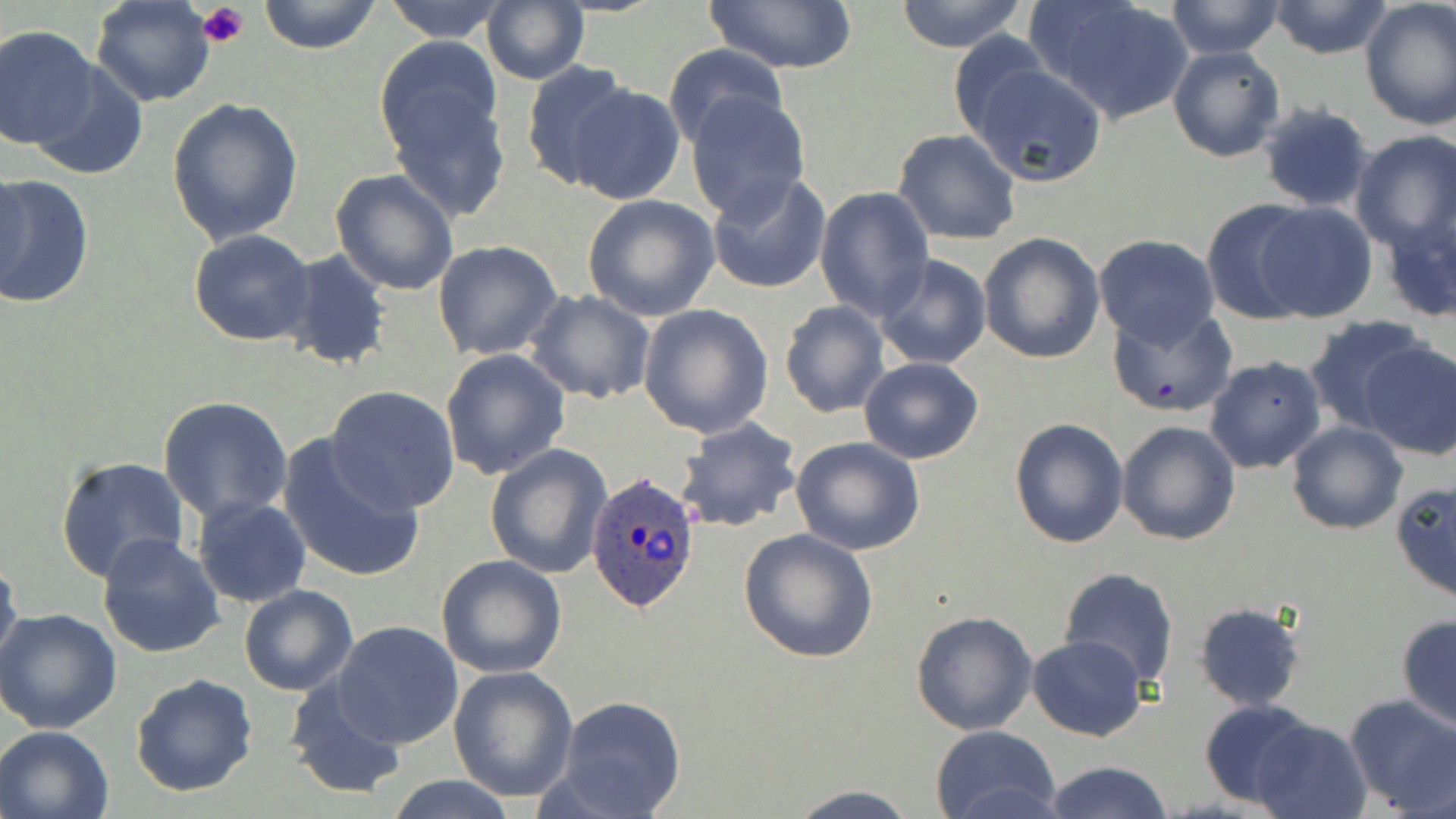

Summary:
  - Coordinate format: approximate bounding boxes as (x1,y1)-(x2,y2) corner pairs in pixels
  - Platelet locations: (197,1)-(249,48)
  - Plasmodium ovale-infected red blood cell locations (subset): (587,471)-(703,612)
  - Uninfected red blood cell locations (subset): (91,0)-(216,107), (258,0)-(380,55), (893,0)-(1030,52), (1032,0)-(1194,123), (1164,0)-(1285,58), (379,1)-(507,44), (480,1)-(590,87), (703,1)-(859,75), (1267,1)-(1394,59), (1358,1)-(1456,130), (960,14)-(1174,167), (0,25)-(99,151), (947,32)-(1056,143), (374,35)-(505,165), (661,44)-(788,151), (1168,46)-(1287,163), (963,58)-(1109,188), (29,59)-(149,179), (519,60)-(639,190), (379,79)-(512,223), (562,83)-(685,205), (685,92)-(810,221), (166,96)-(303,248), (1258,102)-(1375,212), (892,128)-(1021,244), (1350,132)-(1456,250), (330,168)-(459,297), (707,171)-(834,295), (0,173)-(94,310), (814,185)-(936,323), (581,194)-(721,322), (1201,199)-(1319,325), (1254,202)-(1377,323), (189,229)-(315,346), (978,231)-(1106,363), (1092,235)-(1222,349), (431,239)-(563,361), (277,250)-(391,372), (873,255)-(992,371), (525,290)-(656,405), (779,300)-(890,419), (637,303)-(773,438), (1107,306)-(1239,418), (1301,314)-(1434,433), (1358,339)-(1456,461), (439,349)-(571,482), (1205,356)-(1327,475), (857,357)-(985,464), (325,385)-(460,512), (158,395)-(293,522), (675,417)-(802,533), (1008,417)-(1129,548), (1115,420)-(1241,545), (1285,421)-(1408,535), (278,434)-(427,584), (791,437)-(925,555), (486,443)-(613,578), (56,455)-(189,585), (1390,480)-(1456,603), (191,495)-(312,609), (738,527)-(880,664), (96,532)-(226,659), (436,554)-(567,678), (0,555)-(22,673), (1058,566)-(1180,688), (238,585)-(358,697), (1194,602)-(1306,710), (0,608)-(123,734), (910,609)-(1040,736), (1396,615)-(1456,730), (332,621)-(464,749), (1026,635)-(1147,741), (447,664)-(579,802), (129,672)-(258,796), (283,678)-(406,800), (1346,694)-(1456,817), (553,695)-(688,818), (1198,698)-(1320,809), (1250,718)-(1372,819), (0,725)-(114,819), (930,726)-(1061,819), (1042,760)-(1172,819), (385,775)-(520,818), (785,785)-(922,819)
  - Slide-level diagnosis: Plasmodium ovale
  - Preparation: thin blood smear
  - Modality: optical microscopy
  - Stain: May-Grünwald-Giemsa
  - Image size: 1456×819 pixels
  - Magnification: 1000x
  - Field of view: one of a larger specimen